Name the blood parasite species.
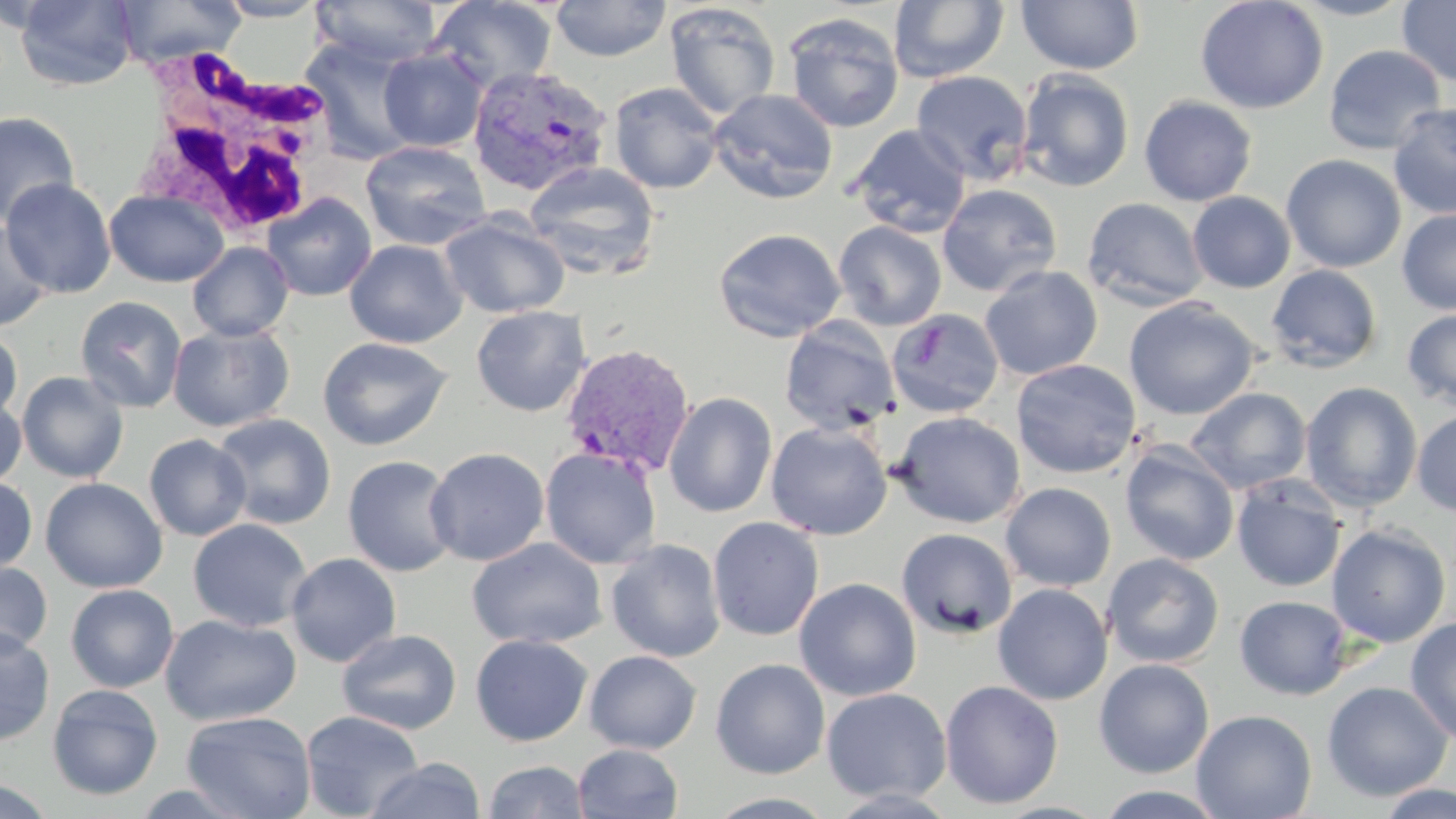
Plasmodium vivax.

field of view = single
modality = light microscopy
Plasmodium vivax-infected red blood cell locations = approximate bounding boxes as (x1, y1, x2, y2) in pixels: (467, 65, 614, 198), (559, 343, 696, 477)
uninfected red blood cell locations = approximate bounding boxes as (x1, y1, x2, y2) in pixels: (15, 0, 139, 91), (113, 0, 246, 69), (215, 0, 329, 21), (311, 0, 441, 68), (429, 0, 558, 93), (550, 0, 672, 61), (1015, 0, 1144, 74), (1194, 0, 1329, 115), (1288, 0, 1419, 21), (888, 1, 1010, 84), (1397, 1, 1456, 87), (664, 3, 781, 120), (782, 12, 905, 133), (300, 38, 422, 163), (1323, 44, 1446, 155), (378, 47, 488, 152), (1015, 68, 1135, 192), (910, 70, 1034, 185), (608, 82, 724, 194), (1019, 87, 1259, 198), (707, 88, 838, 205), (1139, 95, 1257, 206), (1388, 102, 1456, 219), (0, 110, 80, 227), (848, 124, 971, 238), (360, 140, 491, 251), (1281, 154, 1407, 273), (525, 161, 661, 281), (2, 178, 116, 298), (938, 183, 1063, 297), (104, 189, 229, 287), (1188, 191, 1296, 294), (262, 192, 377, 302), (1082, 197, 1209, 311), (1397, 209, 1455, 315), (440, 212, 569, 318), (0, 221, 54, 332), (833, 221, 947, 331), (713, 228, 847, 343), (344, 239, 467, 348), (187, 242, 294, 341), (1265, 264, 1383, 373), (979, 265, 1102, 381), (75, 295, 187, 413), (1123, 297, 1260, 420), (471, 305, 591, 417), (886, 308, 1005, 418), (1401, 308, 1456, 411), (779, 319, 900, 436), (168, 322, 295, 433), (0, 326, 24, 424), (317, 336, 452, 451), (1010, 359, 1142, 479), (16, 371, 128, 482), (1300, 382, 1423, 512), (1186, 387, 1312, 494), (664, 392, 777, 517), (0, 394, 27, 490), (664, 406, 890, 526), (1412, 409, 1456, 518), (890, 411, 1026, 529), (211, 413, 337, 530), (766, 420, 892, 541), (143, 434, 251, 542), (1119, 444, 1239, 566), (425, 446, 549, 566), (540, 447, 661, 569), (342, 455, 460, 577), (0, 476, 37, 574), (1232, 476, 1346, 592), (39, 477, 168, 593), (1000, 482, 1116, 591), (707, 516, 825, 641), (187, 519, 312, 633), (1326, 524, 1451, 647), (896, 528, 1018, 640), (467, 537, 607, 649), (606, 538, 726, 662), (285, 552, 402, 667), (1102, 553, 1224, 669), (0, 560, 53, 658), (793, 578, 921, 702), (993, 583, 1112, 705), (65, 584, 179, 693), (1235, 595, 1352, 700), (160, 614, 301, 726), (1405, 616, 1456, 745), (0, 627, 55, 746), (337, 629, 462, 735), (470, 634, 593, 746), (584, 650, 702, 754), (710, 658, 830, 779), (1093, 659, 1214, 778), (939, 680, 1064, 809), (1321, 681, 1452, 801), (47, 683, 164, 800), (820, 687, 952, 804), (1191, 709, 1317, 819), (300, 710, 425, 819), (181, 711, 317, 819), (572, 743, 684, 819), (365, 757, 485, 818), (482, 761, 589, 819), (0, 777, 57, 818), (124, 781, 260, 818), (1375, 783, 1456, 819), (1093, 785, 1230, 819)
white blood cell locations = approximate bounding boxes as (x1, y1, x2, y2) in pixels: (137, 54, 341, 242)
stain = May-Grünwald-Giemsa
preparation = thin blood film
image size = 1456×819 pixels
magnification = 1000x